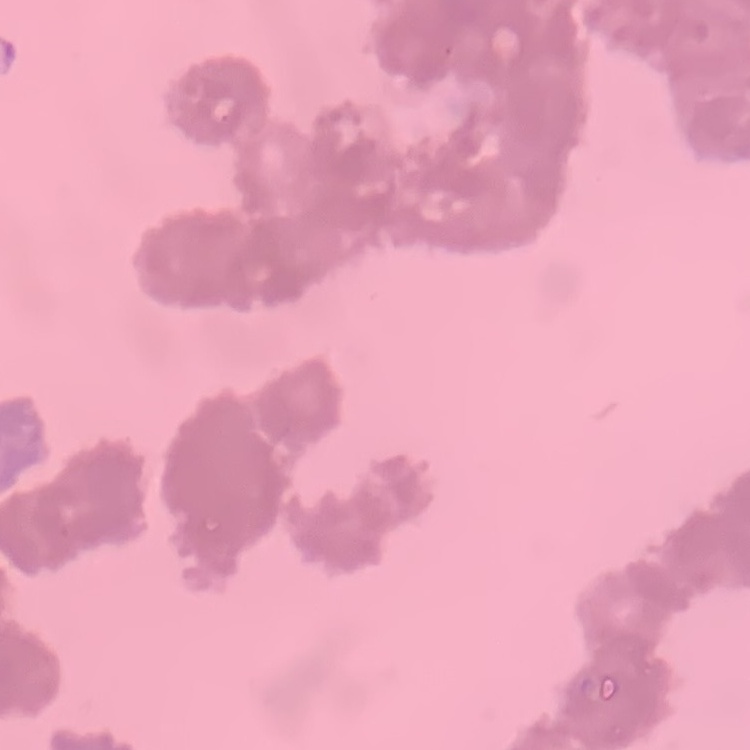

Summary:
  - Erythrocyte morphology: rouleaux formation
  - Preparation: thin blood smear
  - Image type: square crop of a larger photomicrograph
  - Stain: Field's or Giemsa